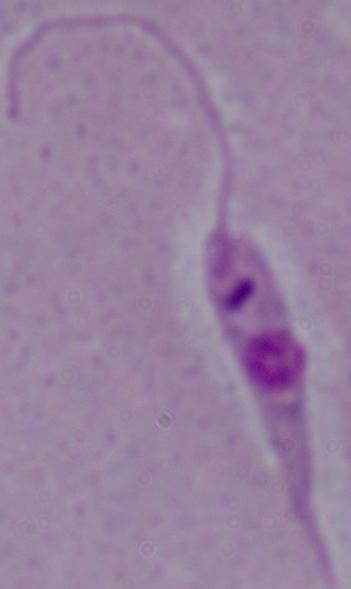

identification = Leishmania
magnification = 1000x
modality = photomicrograph